Locate every leukocyte (white blood cell).
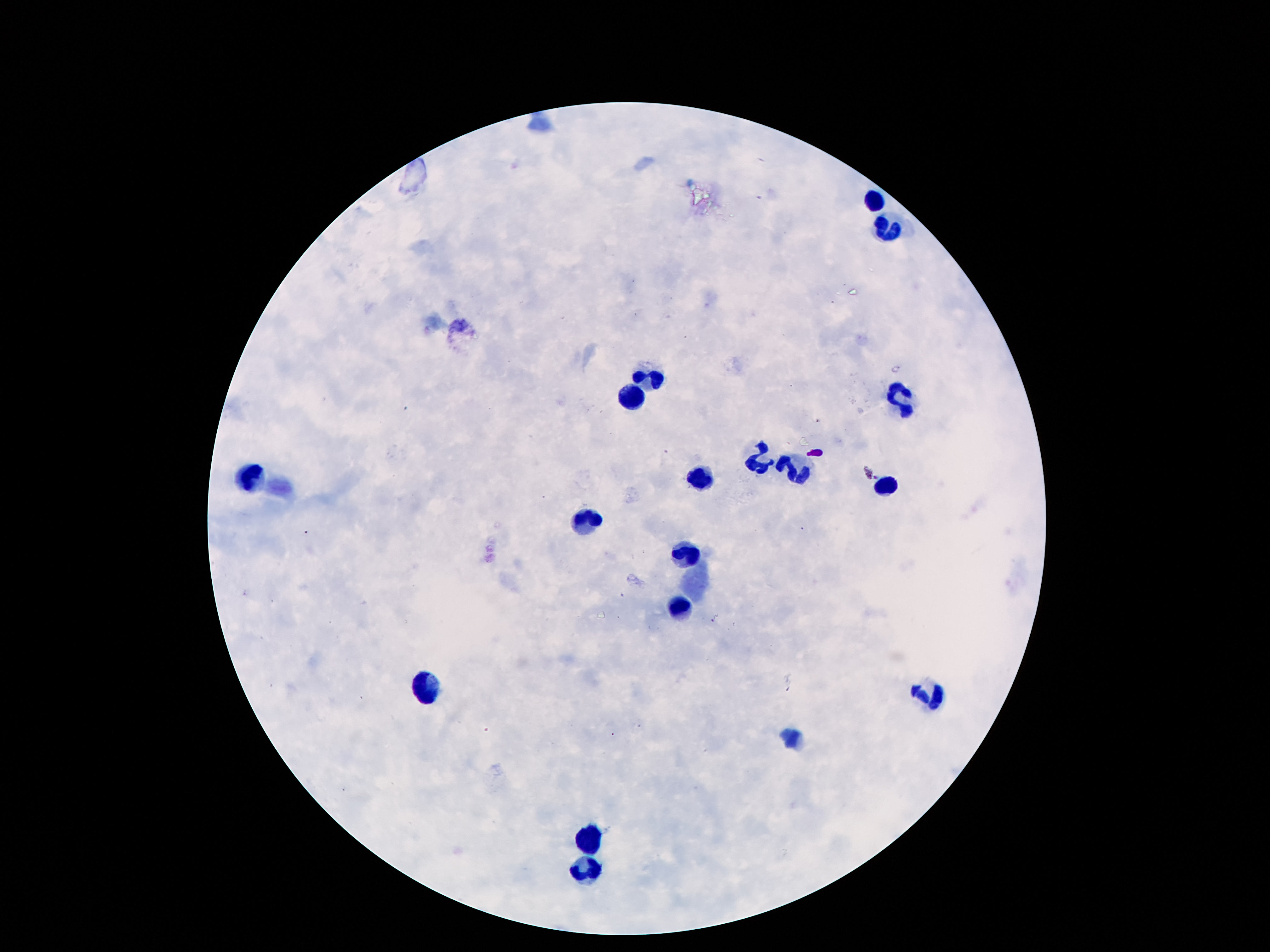

Approximate centers as {x, y} in pixels.
Leukocytes: {874, 197}, {891, 230}, {649, 373}, {897, 393}, {630, 396}, {759, 459}, {796, 470}, {252, 476}, {702, 478}, {883, 481}, {588, 518}, {685, 552}, {681, 609}, {420, 685}, {931, 694}, {590, 839}, {580, 874}.

field of view = single
patient malaria status = negative
image size = 1270×952 pixels
magnification = 100x
stain = Giemsa
capture = smartphone camera through the microscope eyepiece
preparation = thick peripheral-blood smear